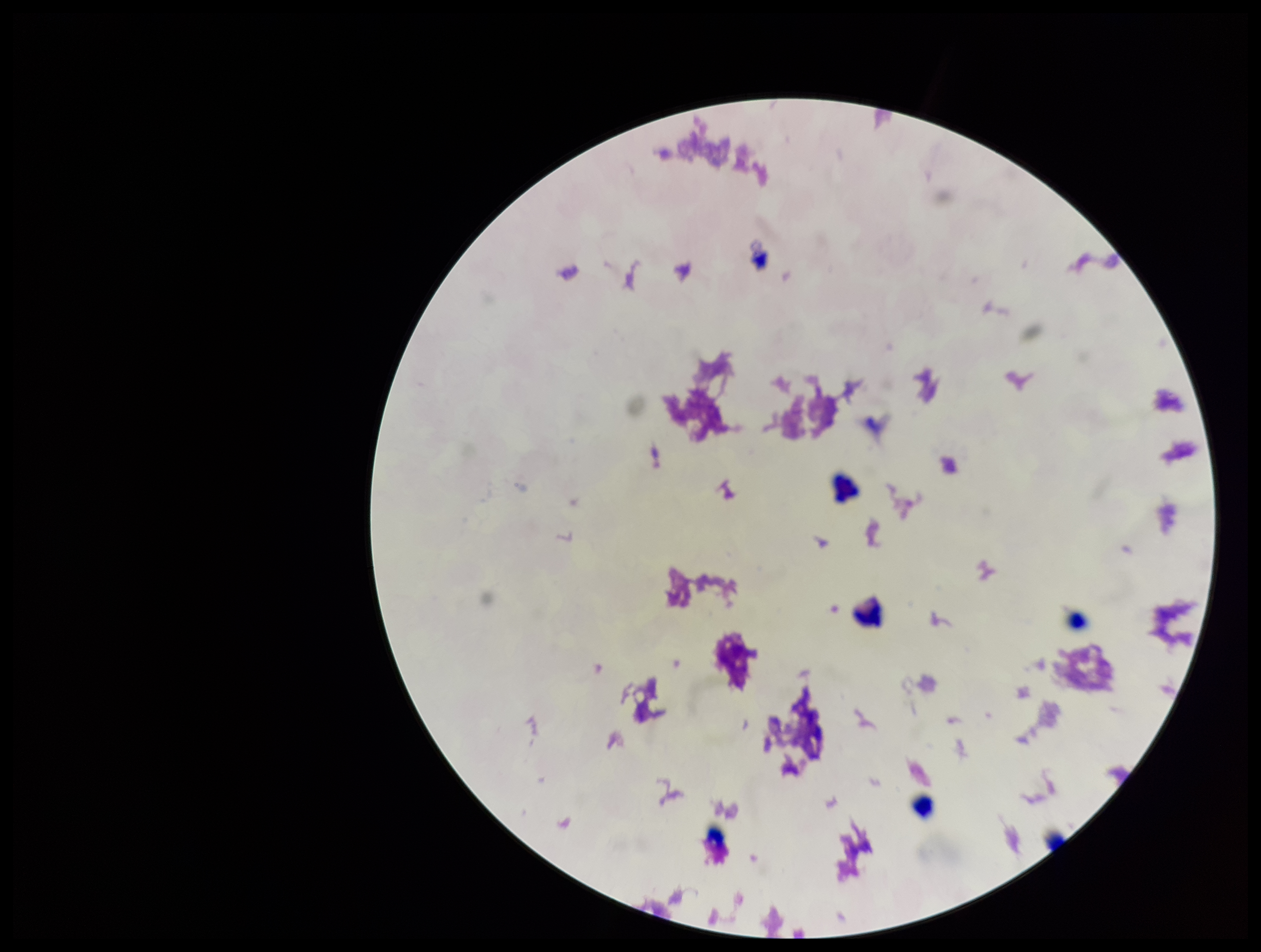
Summary:
  - Parasite count: 0
  - Patient malaria status: negative
  - Leukocyte count: 6
  - Capture: smartphone photograph through the microscope eyepiece
  - Field of view: single
  - Stain: Giemsa
  - Image size: 1261×952 pixels
  - Preparation: thick blood smear
  - Plasmodium parasites: none identified